Identify the cell.
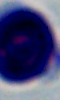

This is a leukocyte.

modality = micrograph
magnification = 1000x